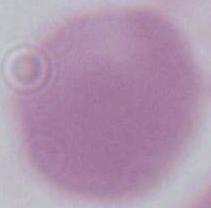
A red blood cell is seen. Captured at 1000x magnification. Photomicrograph.